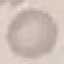
Malaria status: uninfected. Acquired by smartphone through the microscope eyepiece. Automatically extracted cell patch, resized to 64 × 64 pixels. Thin blood film. Giemsa-stained preparation.